Describe the morphology of the red blood cells.
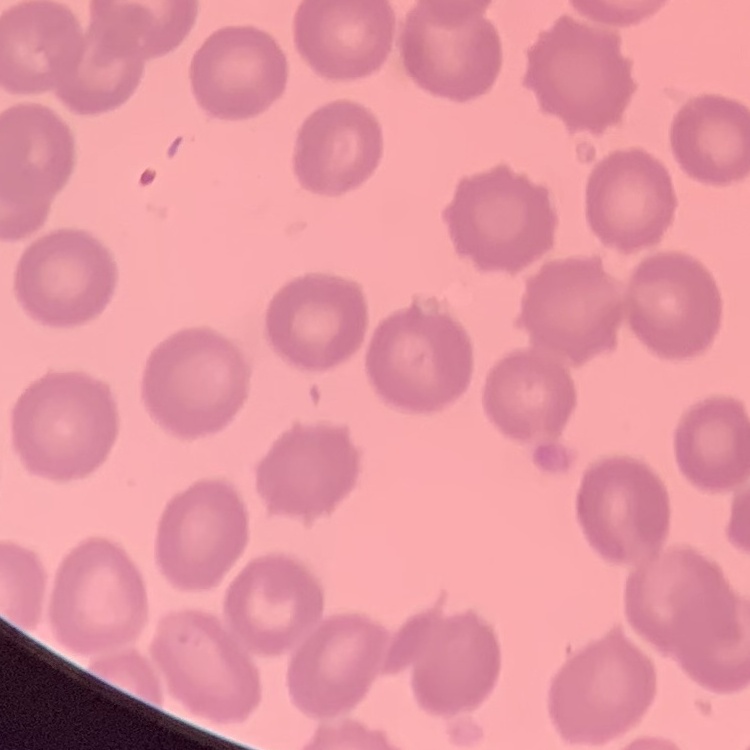
They show no rouleaux formation.

Summary:
  - Preparation: thin blood film
  - Stain: Field's or Giemsa
  - Image type: square crop of a larger photomicrograph